Locate every leukocyte (white blood cell).
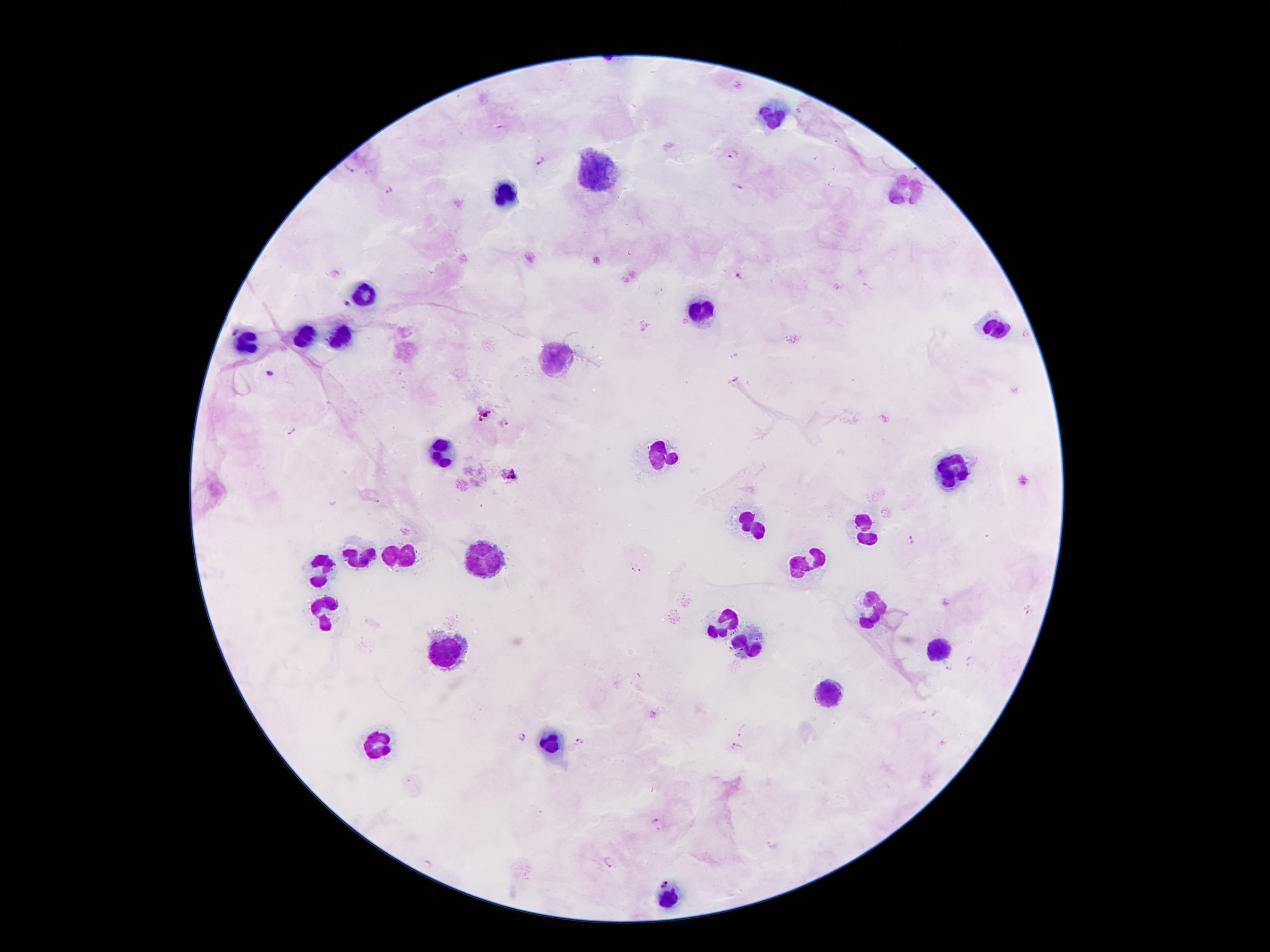
Approximate centers as {x, y} in pixels.
Leukocytes: {773, 114}, {593, 175}, {906, 191}, {504, 196}, {503, 197}, {365, 292}, {702, 313}, {993, 327}, {305, 337}, {343, 339}, {250, 343}, {559, 361}, {559, 362}, {441, 452}, {657, 455}, {949, 472}, {750, 524}, {867, 530}, {479, 549}, {361, 553}, {401, 553}, {317, 564}, {806, 564}, {867, 608}, {323, 614}, {722, 623}, {745, 644}, {449, 648}, {939, 648}, {832, 696}, {548, 742}, {376, 744}, {670, 898}.

Summary:
  - Malaria parasite locations: {732, 154}, {540, 160}, {737, 186}, {389, 189}, {739, 276}, {346, 305}, {236, 331}, {267, 373}, {484, 413}, {503, 422}, {289, 430}, {510, 475}, {911, 540}, {628, 567}, {641, 568}, {1028, 611}, {970, 662}, {947, 666}, {743, 731}, {523, 737}, {580, 741}, {736, 747}, {656, 821}, {609, 861}, {428, 863}, {664, 883}
  - Preparation: thick blood smear
  - Image size: 1270×952 pixels
  - Magnification: 100x
  - Patient malaria status: positive for Plasmodium falciparum
  - Stain: Giemsa
  - Capture: smartphone through the microscope eyepiece
  - Field of view: single